Describe the morphology of the erythrocytes.
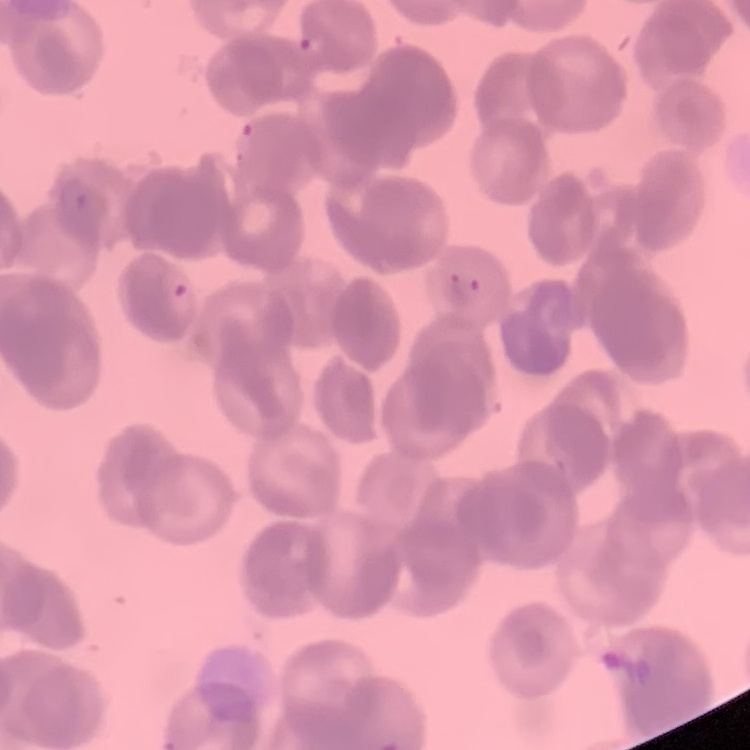

They show rouleaux formation.

Summary:
  - Stain: Field's or Giemsa
  - Preparation: thin blood film
  - Image type: one tile cut from a larger photomicrograph